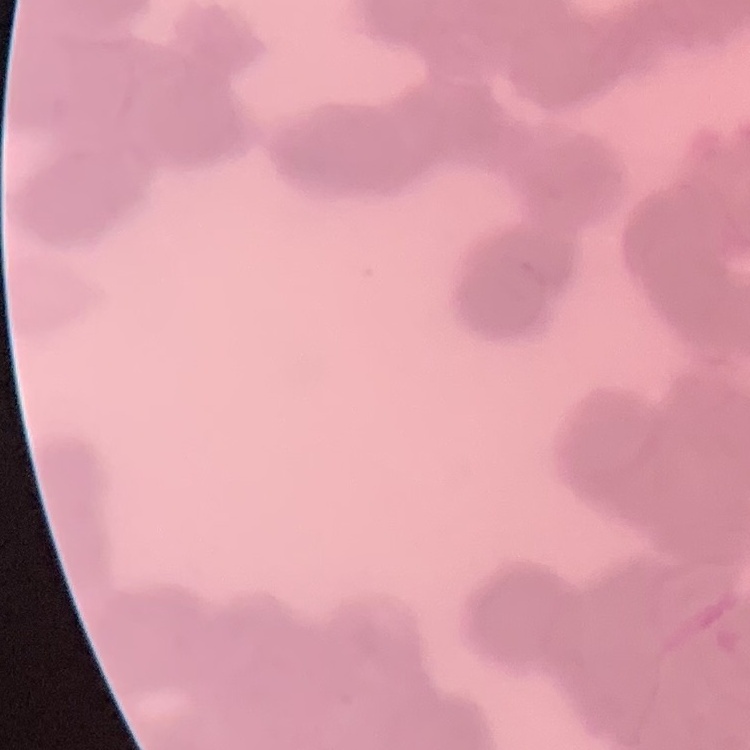 The erythrocytes exhibit rouleaux formation. Thin blood smear. One tile cut from a larger photomicrograph. Stained with either Field's or Giemsa.